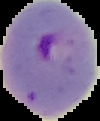
From a thin blood smear. Image is 100×121 pixels. Cell region segmented out of the field of view; the surrounding area is masked to black. Malaria status: parasitized.